Assess this cell for malaria.
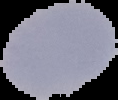

It is uninfected.

{
  "preparation": "thin blood smear",
  "image_size": "118×100 pixels",
  "image_type": "cell region segmented out of the field of view; surrounding area masked to black"
}